State which parasite is depicted.
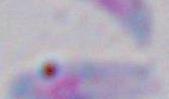

This is Toxoplasma gondii.

Summary:
  - Magnification: 1000x
  - Modality: micrograph